Name the blood parasite species.
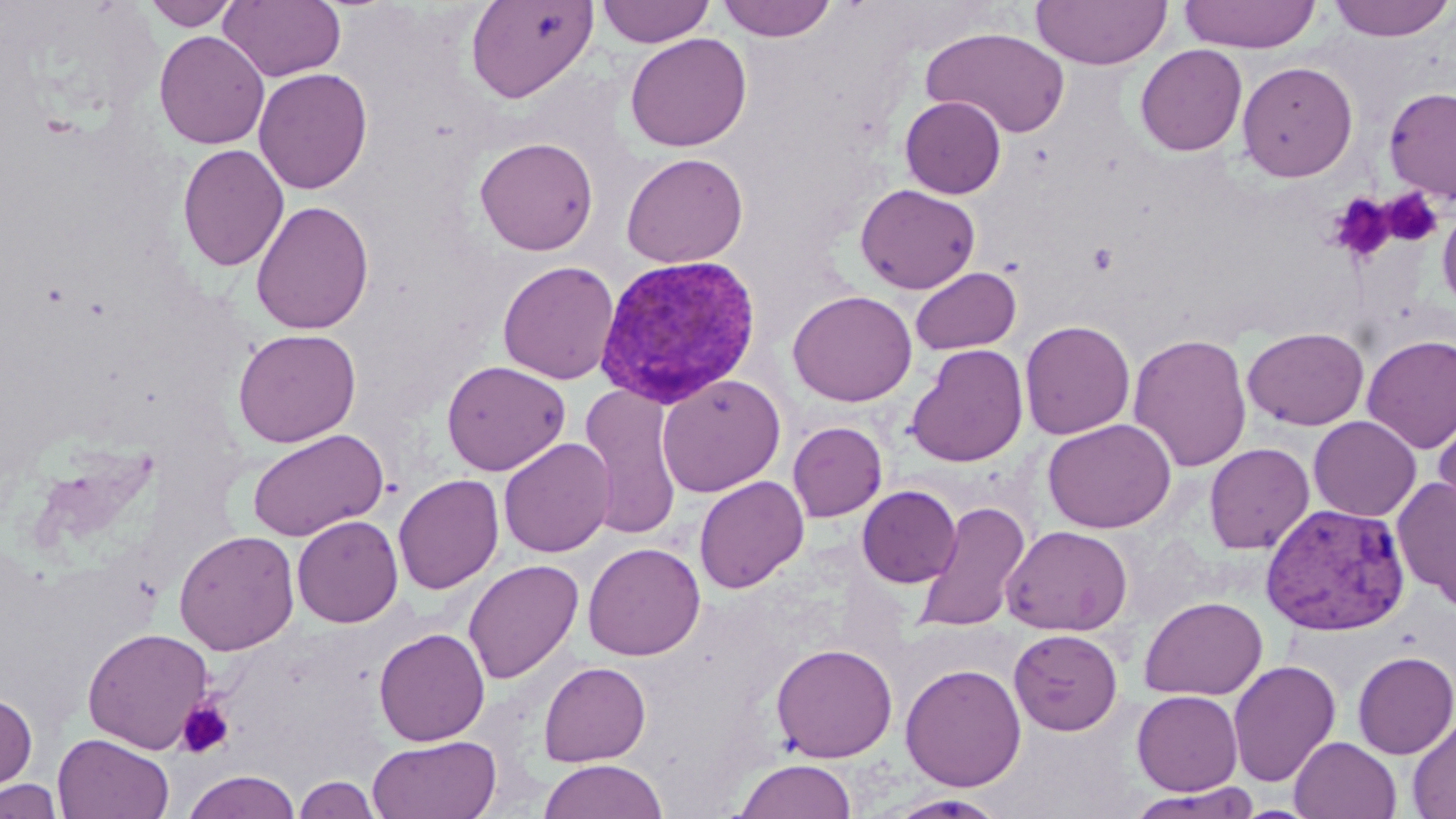

Plasmodium vivax.

Approximate bounding boxes as (x1,y1)-(x2,y2) corner pairs in pixels. Uninfected red blood cell locations: (142,0)-(240,30), (219,0)-(346,82), (465,0)-(598,103), (596,0)-(714,47), (716,0)-(838,42), (1031,0)-(1172,70), (1179,0)-(1321,53), (1328,0)-(1454,43), (921,27)-(1071,139), (154,30)-(269,149), (624,33)-(752,152), (1135,44)-(1247,156), (1236,60)-(1359,182), (254,67)-(373,195), (1382,87)-(1456,203), (900,96)-(1006,199), (475,136)-(599,255), (177,144)-(290,271), (621,152)-(749,268), (855,183)-(981,294), (250,200)-(374,335), (1437,200)-(1456,316), (498,261)-(620,385), (910,266)-(1022,355), (787,289)-(917,407), (1019,319)-(1135,440), (1243,326)-(1369,430), (232,328)-(361,447), (1128,332)-(1252,472), (1361,334)-(1456,453), (906,344)-(1029,467), (441,360)-(571,475), (657,374)-(786,497), (578,384)-(684,540), (1431,403)-(1456,530), (1308,416)-(1421,521), (1042,418)-(1177,534), (788,421)-(887,522), (246,428)-(388,541), (499,438)-(615,557), (1204,442)-(1315,554), (393,474)-(504,594), (694,475)-(809,594), (1393,475)-(1456,611), (856,485)-(962,587), (913,501)-(1031,635), (292,515)-(403,628), (1002,525)-(1133,636), (174,530)-(300,655), (583,542)-(705,661), (463,559)-(583,684), (1139,595)-(1268,700), (82,626)-(214,754), (374,627)-(490,746), (1008,628)-(1123,735), (770,642)-(898,763), (1352,650)-(1456,759), (1228,660)-(1341,787), (538,661)-(651,766), (900,662)-(1026,792), (1131,689)-(1243,795), (0,691)-(38,796), (1407,716)-(1456,818), (53,733)-(175,819), (367,734)-(502,819), (1289,736)-(1401,819), (538,758)-(668,819), (733,758)-(857,818), (181,770)-(302,819), (293,775)-(382,818), (0,777)-(65,819), (1126,785)-(1262,818), (887,793)-(1008,818). Plasmodium vivax-infected red blood cell locations: (593,253)-(763,409), (1260,502)-(1412,637). Platelet locations: (1381,188)-(1443,247), (1327,192)-(1397,264), (1088,243)-(1118,274), (175,699)-(234,759). Optical microscopy. 1000x magnification. Single field of view. Thin blood smear. May-Grünwald-Giemsa stain. Image is 1456×819 pixels.